Classify this cell by malaria status.
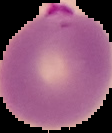
It is parasitized.

Summary:
  - Image type: segmented cell region on a black background
  - Preparation: thin blood smear
  - Image size: 112×133 pixels